Identify the parasite.
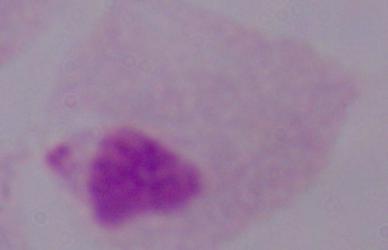
A trichomonad.

Photomicrograph. 1000x magnification.